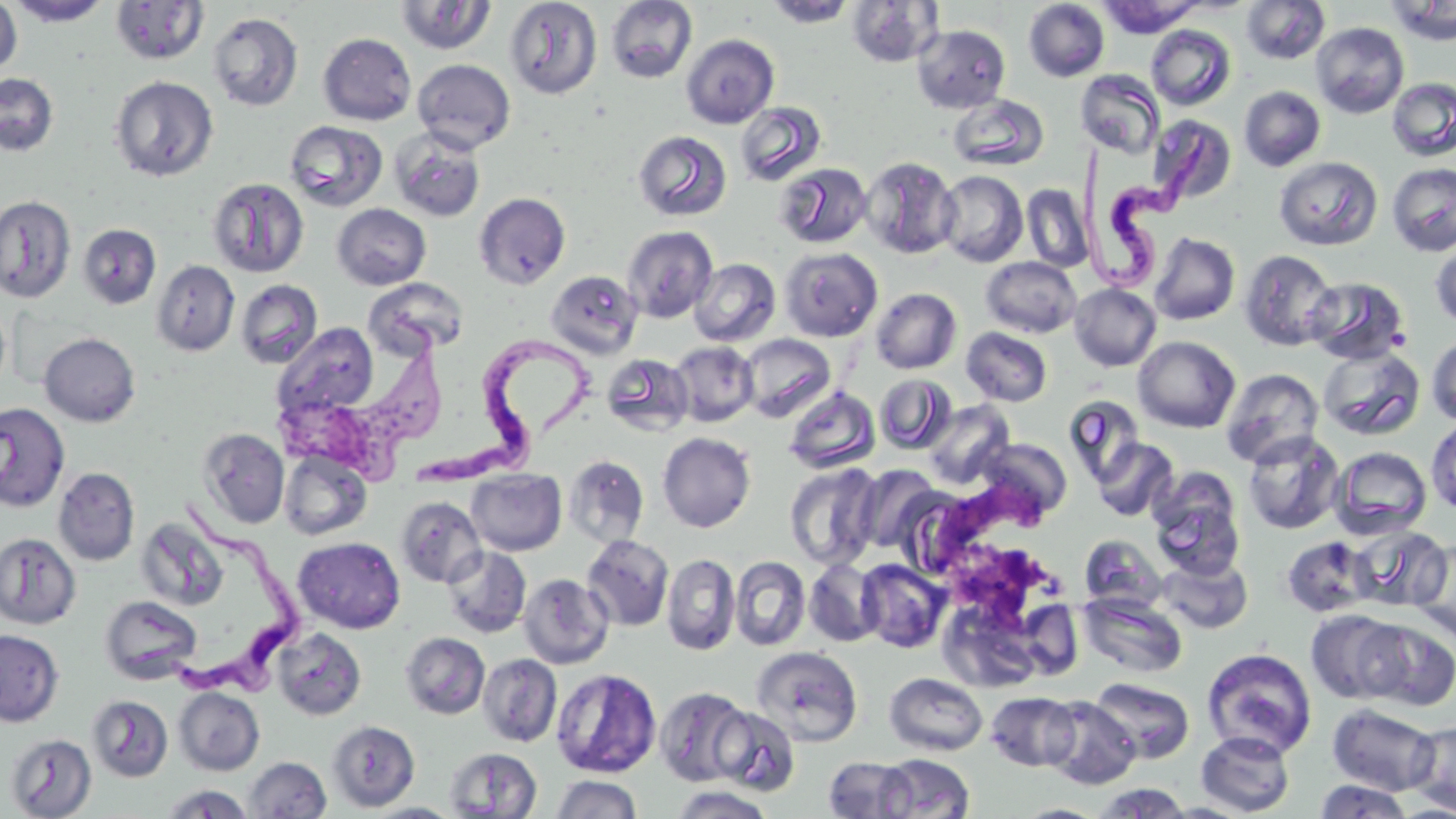

Summary:
  - Coordinate format: approximate bounding boxes as (x1, y1, x2, y2) in pixels
  - Trypanosoma brucei locations: (1059, 120, 1220, 302), (281, 309, 441, 495), (433, 325, 607, 482), (153, 493, 316, 696)
  - Uninfected red blood cell locations: (0, 0, 22, 77), (7, 0, 113, 27), (504, 0, 603, 99), (765, 0, 857, 28), (1023, 0, 1109, 82), (1097, 0, 1205, 36), (1242, 0, 1330, 64), (110, 1, 209, 65), (394, 1, 497, 56), (604, 1, 698, 85), (847, 1, 943, 67), (1387, 1, 1456, 46), (207, 12, 303, 111), (1311, 22, 1409, 118), (912, 24, 1010, 113), (1146, 25, 1235, 110), (318, 33, 417, 125), (680, 34, 779, 129), (412, 59, 516, 154), (1076, 70, 1165, 159), (0, 73, 58, 156), (109, 76, 219, 182), (1386, 77, 1456, 162), (1239, 86, 1326, 171), (948, 94, 1049, 172), (734, 101, 828, 187), (1148, 114, 1237, 207), (285, 120, 388, 212), (390, 129, 486, 222), (633, 130, 732, 222), (632, 131, 725, 323), (860, 156, 960, 259), (1274, 156, 1382, 251), (775, 162, 873, 249), (1386, 163, 1456, 257), (935, 170, 1028, 267), (208, 178, 309, 277), (1022, 184, 1093, 272), (474, 192, 571, 290), (0, 195, 76, 304), (332, 203, 431, 290), (78, 224, 161, 310), (621, 225, 719, 324), (1149, 232, 1240, 325), (1430, 238, 1456, 331), (779, 247, 883, 341), (1239, 249, 1340, 351), (981, 257, 1082, 338), (689, 258, 781, 346), (151, 260, 240, 356), (546, 270, 644, 358), (1304, 276, 1410, 365), (365, 278, 469, 358), (236, 279, 323, 369), (1070, 283, 1161, 372), (871, 288, 962, 374), (0, 301, 10, 395), (272, 323, 379, 420), (961, 327, 1053, 407), (39, 333, 140, 427), (739, 333, 835, 421), (1426, 335, 1456, 426), (1133, 336, 1240, 433), (669, 341, 759, 426), (1317, 346, 1426, 442), (601, 353, 694, 437), (1221, 368, 1325, 468), (874, 373, 958, 455), (784, 385, 879, 473), (1063, 395, 1144, 484), (924, 400, 1016, 489), (0, 402, 70, 512), (1426, 417, 1456, 515), (197, 428, 290, 528), (1242, 431, 1347, 535), (657, 432, 756, 533), (977, 437, 1072, 521), (1091, 437, 1179, 522), (1330, 447, 1433, 539), (278, 451, 372, 541), (564, 455, 649, 547), (784, 463, 882, 570), (855, 464, 943, 554), (53, 467, 140, 566), (466, 468, 567, 556), (1148, 469, 1245, 578), (396, 496, 487, 588), (136, 517, 229, 612), (1351, 524, 1452, 612), (0, 533, 81, 629), (581, 534, 674, 631), (1079, 534, 1166, 613), (1281, 535, 1374, 617), (293, 537, 405, 633), (1409, 539, 1456, 641), (442, 545, 532, 638), (662, 553, 740, 656), (1156, 554, 1253, 634), (730, 556, 811, 651), (804, 558, 885, 647), (856, 559, 950, 653), (519, 573, 614, 669), (1079, 593, 1187, 679), (100, 595, 201, 683), (1305, 609, 1406, 704), (1361, 619, 1456, 711), (272, 628, 366, 720), (0, 629, 64, 727), (401, 632, 490, 719), (750, 645, 863, 746), (1202, 648, 1318, 759), (478, 654, 562, 747), (551, 668, 661, 778), (884, 673, 988, 756), (1090, 677, 1194, 763), (174, 687, 264, 775), (655, 687, 753, 786), (985, 691, 1081, 772), (88, 695, 174, 781), (1041, 696, 1140, 790), (1327, 703, 1439, 795), (712, 706, 801, 796), (328, 720, 420, 811), (1407, 721, 1456, 814), (1195, 730, 1296, 816), (5, 733, 97, 817), (444, 747, 543, 818), (877, 753, 975, 818), (245, 756, 331, 818), (823, 756, 914, 818), (551, 774, 642, 819), (1314, 778, 1412, 818), (1092, 783, 1194, 818), (159, 784, 255, 818), (670, 786, 775, 818), (363, 802, 464, 819), (1015, 803, 1106, 818)
  - Slide-level diagnosis: Trypanosoma brucei
  - Image size: 1456×819 pixels
  - Preparation: thin blood smear
  - Modality: optical microscopy
  - Magnification: 1000x
  - Stain: May-Grünwald-Giemsa
  - Field of view: one of a larger specimen